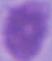
Summary:
  - Identification: red blood cell
  - Magnification: 1000x
  - Modality: photomicrograph